Classify this cell by malaria status.
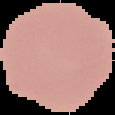
Uninfected.

preparation: thin blood smear
image_size: 115×115 pixels
image_type: segmented cell region with the area outside set to black